Report the malaria status of this cell.
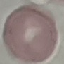
It is uninfected.

Automatically extracted cell patch, resized to 64 × 64 pixels. Thin blood film. Photographed with a smartphone camera at the microscope eyepiece. Giemsa-stained preparation.